Assess the morphology of the red blood cells.
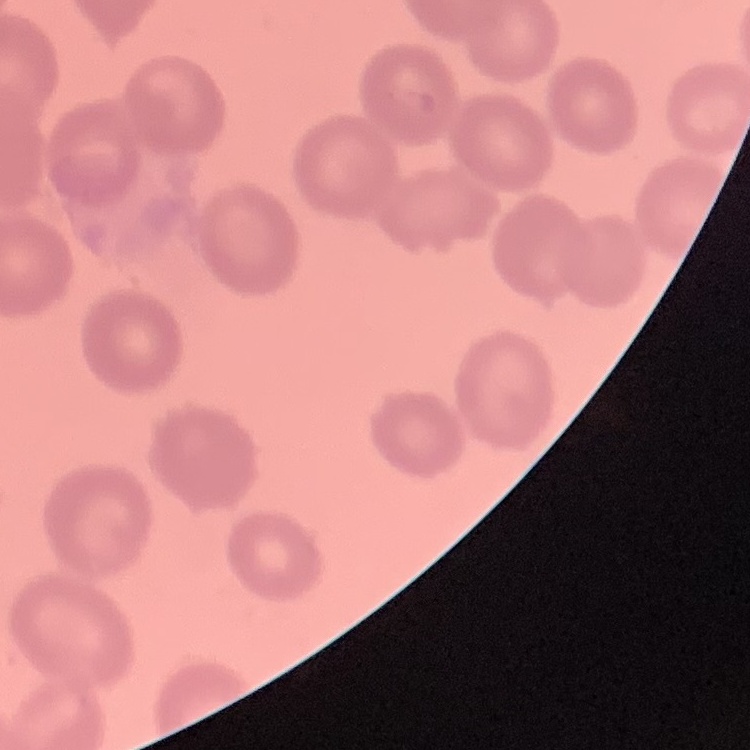
No rouleaux formation.

{
  "preparation": "thin blood film",
  "image_type": "square crop of a larger photomicrograph",
  "stain": "Field's or Giemsa"
}